Classify this cell by malaria status.
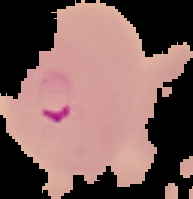
Parasitized.

Image is 193×199 pixels. Cell region segmented out of the field of view; the surrounding area is masked to black. From a thin blood film.